Describe the morphology of the red blood cells.
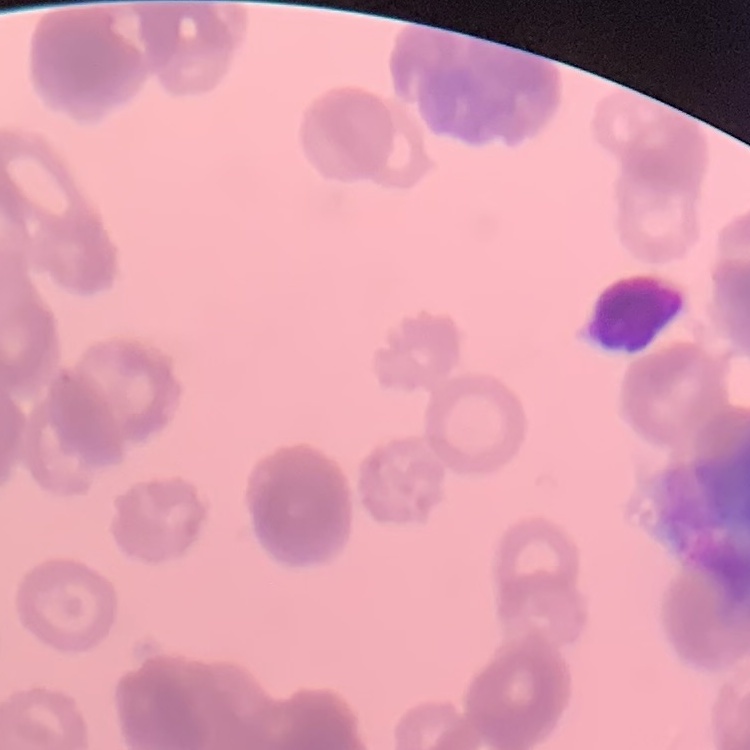

Rouleaux formation.

One tile cut from a larger photomicrograph. Thin blood film. Field's or Giemsa stain.